Classify this cell by malaria status.
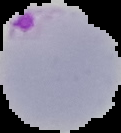

Parasitized.

Image is 121×133 pixels. The area outside the segmented cell region is set to black. From a thin blood film.